Comment on the morphology of the erythrocytes.
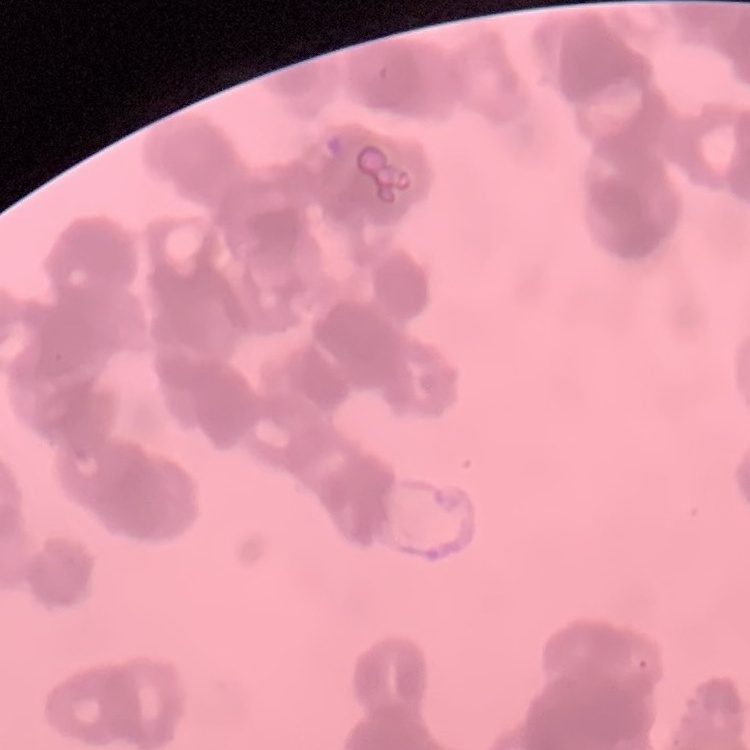
They show rouleaux formation.

{
  "preparation": "thin peripheral smear",
  "stain": "Field's or Giemsa",
  "image_type": "square crop of a larger photomicrograph"
}